Classify this cell by malaria status.
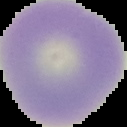
It is uninfected.

image type = segmented cell region on a black background
preparation = thin blood film
image size = 127×127 pixels